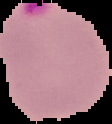
Summary:
  - Image size: 112×124 pixels
  - Preparation: thin blood film
  - Image type: segmented cell region with the area outside set to black
  - Malaria status: parasitized